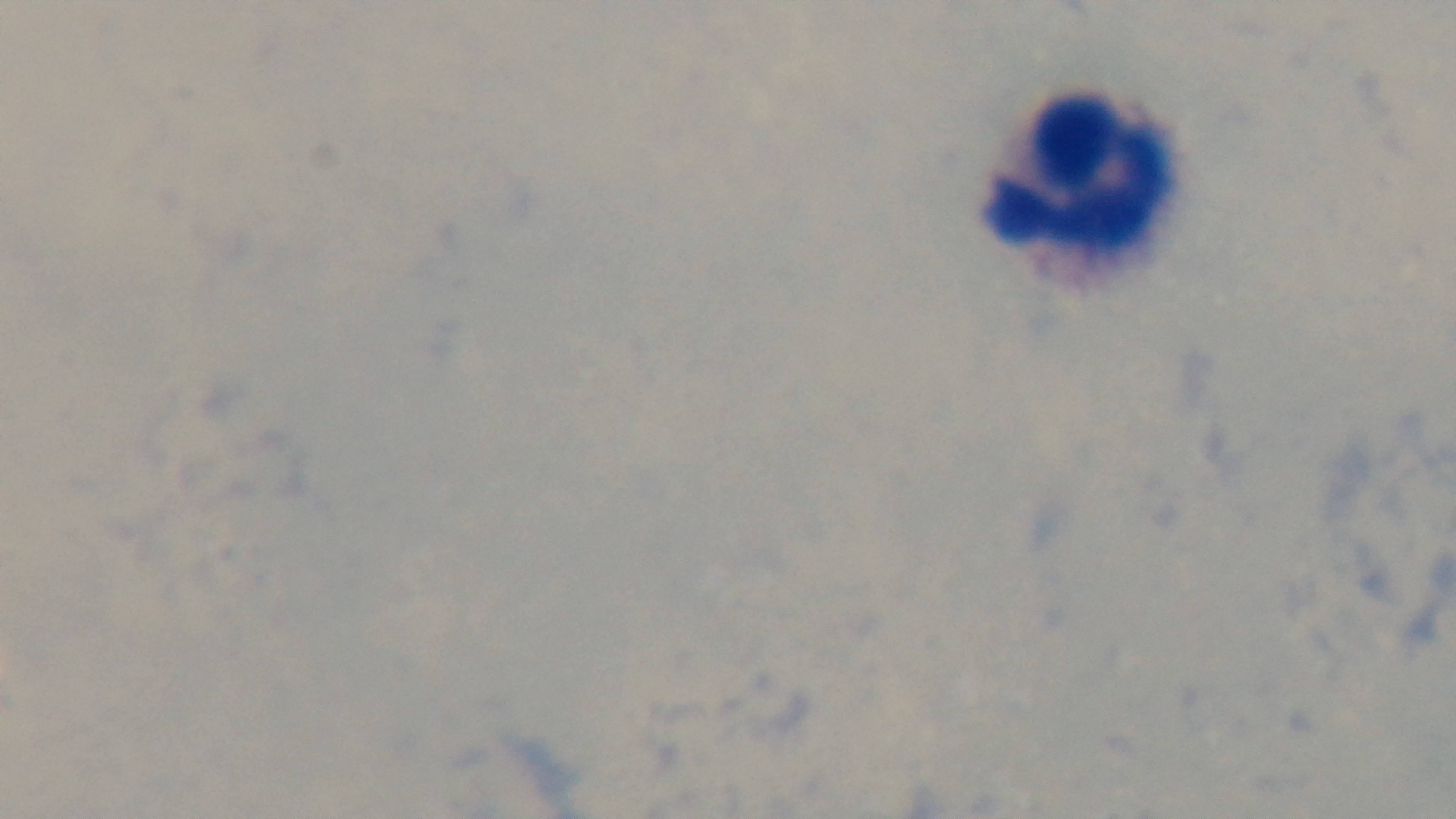
Summary:
  - Malaria status: negative
  - Capture: mounted 4K digital camera
  - Stain: Giemsa
  - Modality: light microscopy
  - Field of view: one from the slide
  - Objective: 100x oil immersion
  - Preparation: thick smear